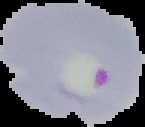

Summary:
  - Image type: segmented cell region on a black background
  - Preparation: thin blood smear
  - Image size: 145×127 pixels
  - Malaria status: parasitized